Report the malaria status of this cell.
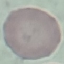

It is uninfected.

Summary:
  - Stain: Giemsa
  - Image type: cell patch, automatically extracted from a larger field of view and resized to 64 × 64 pixels
  - Preparation: thin blood film
  - Capture: smartphone camera at the microscope eyepiece